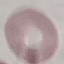 Result: no malaria parasites seen. Automatically extracted cell patch, resized to 64 × 64 pixels. Acquired by smartphone through the microscope eyepiece. Giemsa-stained preparation. Thin blood film.